Locate every leukocyte (white blood cell).
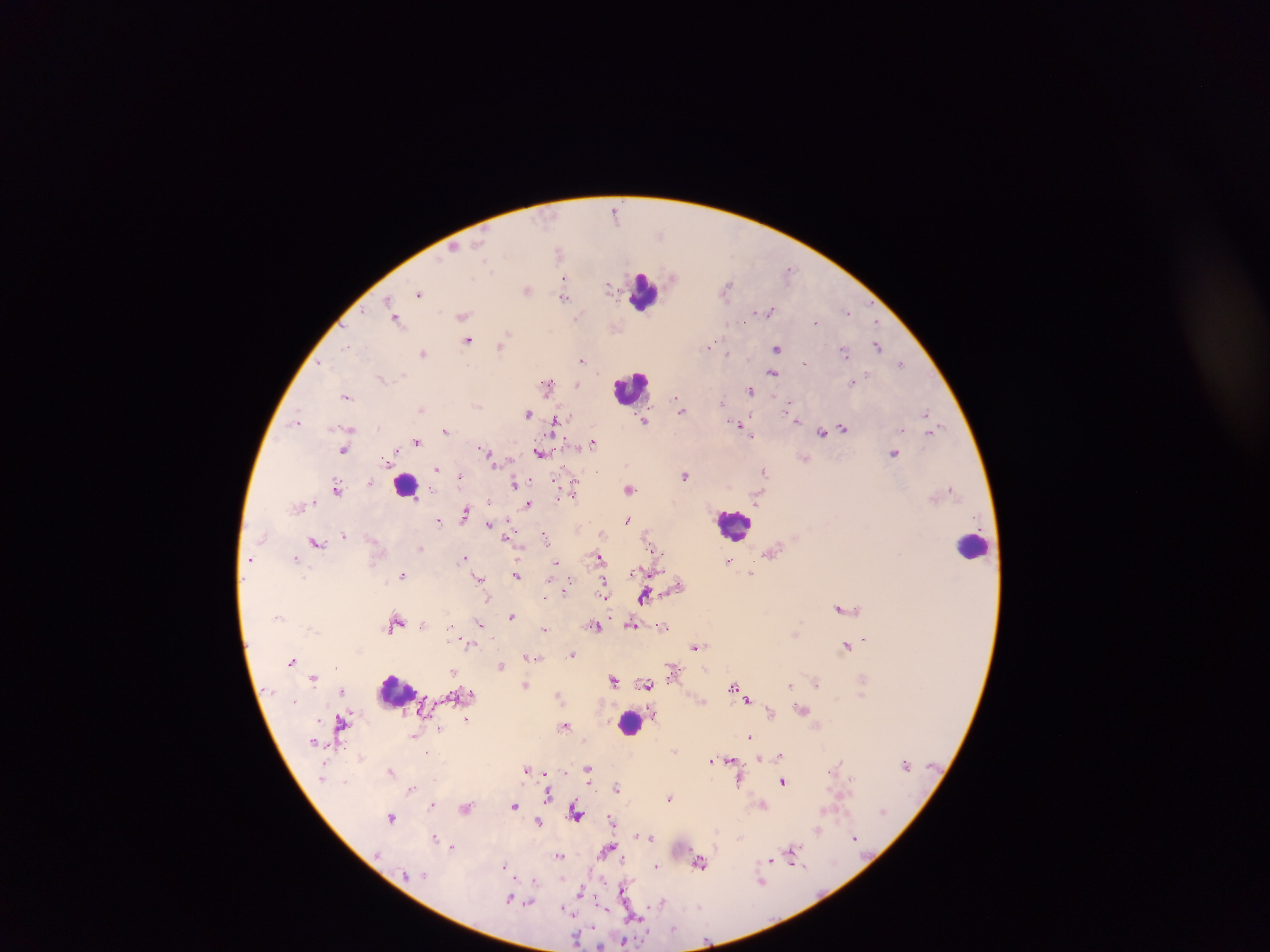

Approximate centers as x y in pixels.
Leukocytes: 645 294; 631 387; 406 489; 734 525; 973 546; 395 693; 630 722.

Summary:
  - Plasmodium parasite locations: 615 210; 660 234; 454 247; 558 251; 487 265; 788 270; 673 276; 565 279; 609 287; 727 287; 526 289; 420 294; 565 296; 387 301; 769 310; 847 311; 363 313; 463 316; 576 318; 396 319; 816 322; 506 334; 468 341; 711 345; 878 345; 347 346; 501 346; 776 348; 843 351; 423 353; 727 353; 582 360; 804 361; 323 363; 901 363; 773 373; 403 375; 381 378; 853 382; 578 384; 548 385; 751 391; 347 396; 677 399; 724 401; 477 406; 788 407; 421 409; 681 410; 927 412; 528 414; 561 418; 297 420; 645 420; 796 420; 554 421; 739 425; 378 426; 843 428; 445 430; 933 431; 822 434; 751 435; 417 441; 594 442; 344 449; 483 450; 539 452; 894 453; 490 455; 804 458; 438 469; 764 472; 685 475; 459 478; 555 481; 515 483; 337 487; 630 489; 951 489; 574 490; 558 496; 571 496; 758 497; 488 502; 529 504; 465 513; 440 520; 627 520; 488 524; 344 536; 506 538; 545 538; 316 542; 420 548; 655 551; 772 552; 295 557; 250 558; 463 558; 600 558; 729 562; 556 563; 752 573; 517 574; 403 575; 479 579; 603 582; 567 587; 606 593; 645 596; 545 597; 607 598; 839 608; 511 616; 396 624; 480 624; 632 624; 596 625; 664 627; 449 628; 545 629; 865 638; 468 646; 696 646; 847 647; 571 655; 530 657; 293 661; 502 665; 336 667; 453 671; 672 674; 313 678; 614 680; 816 682; 647 684; 525 685; 790 685; 733 687; 343 691; 471 694; 558 695; 748 699; 803 709; 771 712; 467 720; 342 721; 565 726; 440 728; 413 737; 749 737; 675 750; 780 754; 361 757; 760 758; 730 759; 712 760; 837 766; 588 768; 391 770; 526 770; 546 774; 589 776; 740 782; 784 782; 617 788; 411 790; 548 795; 669 797; 763 804; 432 805; 515 806; 466 808; 576 812; 391 817; 611 819; 538 822; 818 831; 435 836; 637 836; 651 837; 739 838; 855 838; 453 847; 608 848; 793 851; 559 855; 771 860; 700 863; 506 865; 657 866; 534 880; 762 882; 624 888; 581 892; 510 899; 519 900; 661 901; 529 903; 637 915; 674 929; 577 938; 623 941
  - Country: Ghana
  - Field of view: single
  - Capture: mobile-phone photograph through a microscope
  - Image size: 1270×952 pixels
  - Preparation: thick blood smear